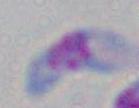 Toxoplasma gondii is shown. Micrograph. 1000x magnification.